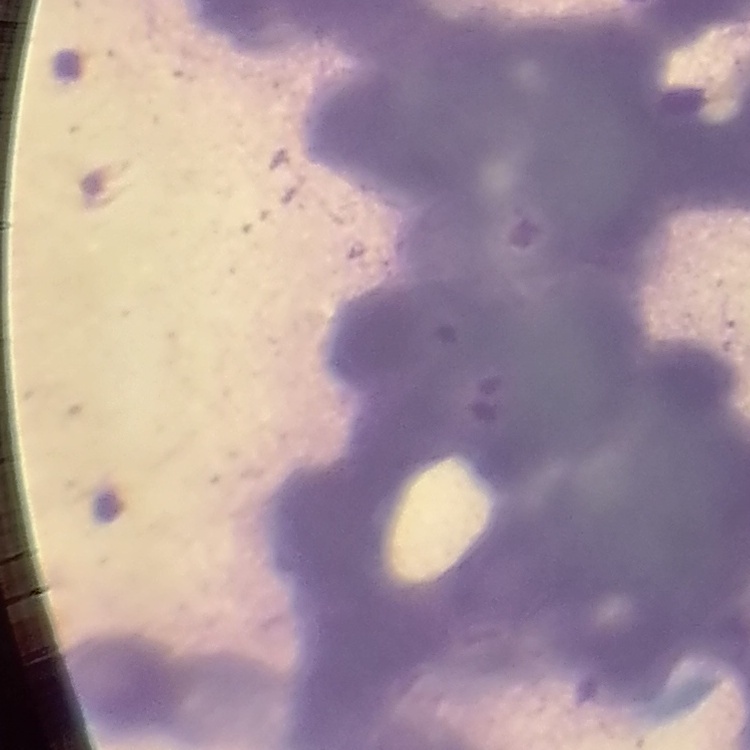

erythrocyte_morphology: rouleaux formation
image_type: one tile cut from a larger photomicrograph
stain: Field's or Giemsa
preparation: thin blood smear